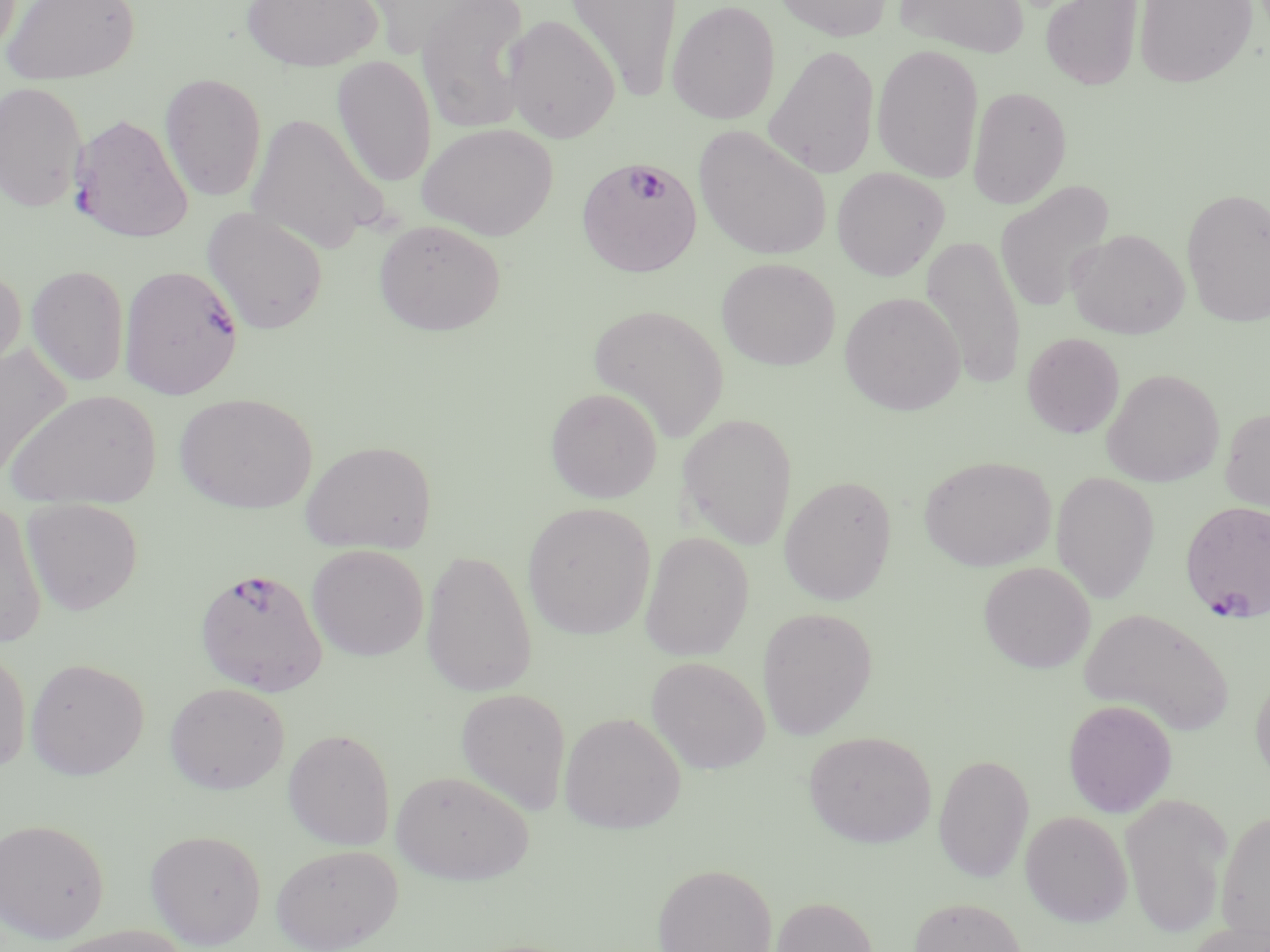
Summary:
  - Coordinate format: approximate bounding boxes as [x1, y1, x2, y2] in pixels
  - Uninfected red blood cell locations: [1, 0, 141, 86], [239, 0, 384, 72], [564, 0, 683, 100], [667, 0, 780, 125], [771, 0, 894, 42], [892, 0, 1030, 58], [1040, 0, 1144, 91], [1133, 0, 1258, 88], [359, 1, 501, 58], [417, 1, 532, 133], [503, 14, 621, 143], [763, 44, 880, 180], [871, 44, 984, 184], [331, 56, 437, 188], [159, 73, 267, 202], [0, 81, 88, 212], [967, 85, 1072, 208], [246, 112, 390, 255], [69, 114, 194, 244], [417, 123, 559, 241], [694, 126, 833, 261], [831, 167, 949, 281], [995, 180, 1116, 312], [1181, 187, 1270, 328], [201, 207, 329, 335], [373, 219, 506, 337], [1067, 228, 1190, 339], [920, 234, 1026, 390], [716, 257, 840, 370], [0, 264, 27, 384], [26, 264, 130, 387], [839, 291, 966, 416], [588, 304, 729, 441], [1022, 332, 1125, 438], [1, 343, 71, 482], [1101, 368, 1224, 487], [545, 386, 663, 503], [6, 389, 162, 509], [174, 393, 317, 514], [1220, 405, 1270, 514], [677, 413, 797, 551], [300, 439, 436, 554], [919, 456, 1055, 572], [1051, 472, 1160, 603], [779, 474, 898, 606], [21, 498, 143, 615], [0, 499, 47, 647], [522, 502, 655, 639], [640, 531, 754, 661], [306, 544, 429, 661], [421, 549, 537, 697], [978, 561, 1096, 673], [1078, 606, 1234, 736], [757, 607, 878, 740], [0, 644, 32, 776], [646, 656, 770, 773], [25, 657, 149, 780], [1250, 667, 1270, 789], [164, 682, 290, 794], [455, 688, 571, 815], [1063, 699, 1178, 817], [559, 712, 686, 834], [282, 728, 395, 851], [804, 730, 936, 848], [933, 753, 1034, 883], [391, 769, 535, 885], [1120, 792, 1233, 937], [1216, 807, 1270, 945], [1020, 811, 1133, 927], [0, 818, 110, 944], [145, 829, 266, 949], [271, 843, 403, 951], [651, 862, 778, 952], [770, 896, 877, 952], [909, 896, 1027, 952], [1185, 920, 1269, 952], [44, 924, 196, 952]
  - Plasmodium falciparum-infected red blood cell locations: [576, 155, 702, 277], [119, 264, 244, 400], [1180, 500, 1270, 620], [194, 566, 328, 697]
  - Slide-level diagnosis: Plasmodium falciparum
  - Field of view: one of a larger specimen
  - Preparation: thin blood smear
  - Stain: May-Grünwald-Giemsa
  - Magnification: 1000x
  - Image size: 1270×952 pixels
  - Modality: optical microscopy